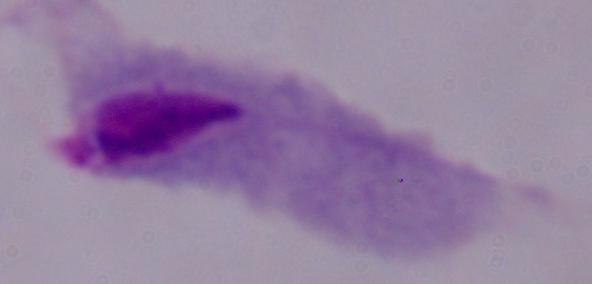
Summary:
  - Modality: photomicrograph
  - Magnification: 1000x
  - Identification: trichomonad